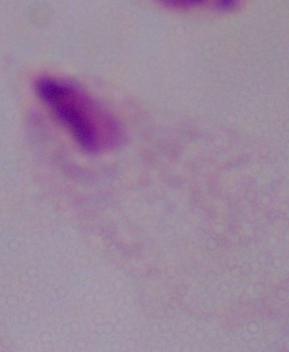

1000x magnification. Photomicrograph. A trichomonad is shown.